Describe the morphology of the erythrocytes.
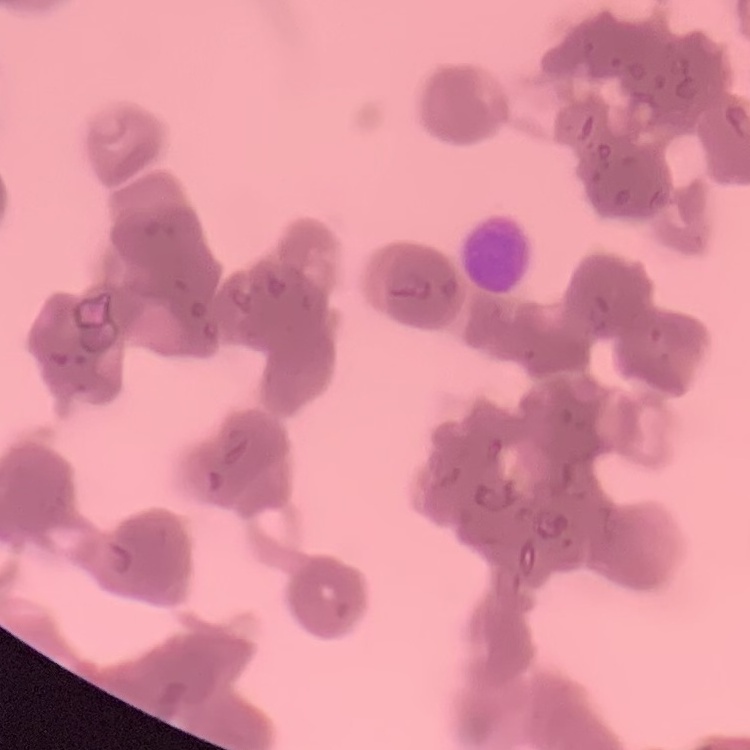
Rouleaux formation.

image type = square crop of a larger photomicrograph
stain = Field's or Giemsa
preparation = thin peripheral smear